Assess this cell for malaria.
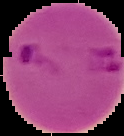

It is parasitized.

From a thin blood film. Segmented cell region on a black background. Image is 124×136 pixels.